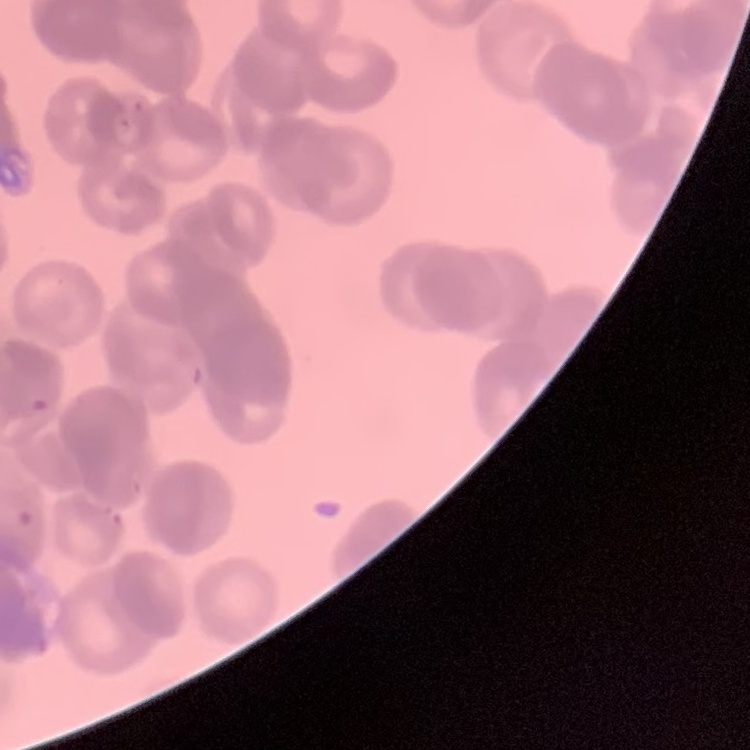
Summary:
  - Erythrocyte morphology: rouleaux formation
  - Image type: one tile cut from a larger photomicrograph
  - Preparation: thin blood smear
  - Stain: Field's or Giemsa